Report the malaria status of this cell.
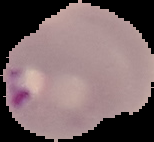

It is parasitized.

From a thin blood film. The area outside the segmented cell region is set to black. Image is 154×142 pixels.